Identify the preparation type.
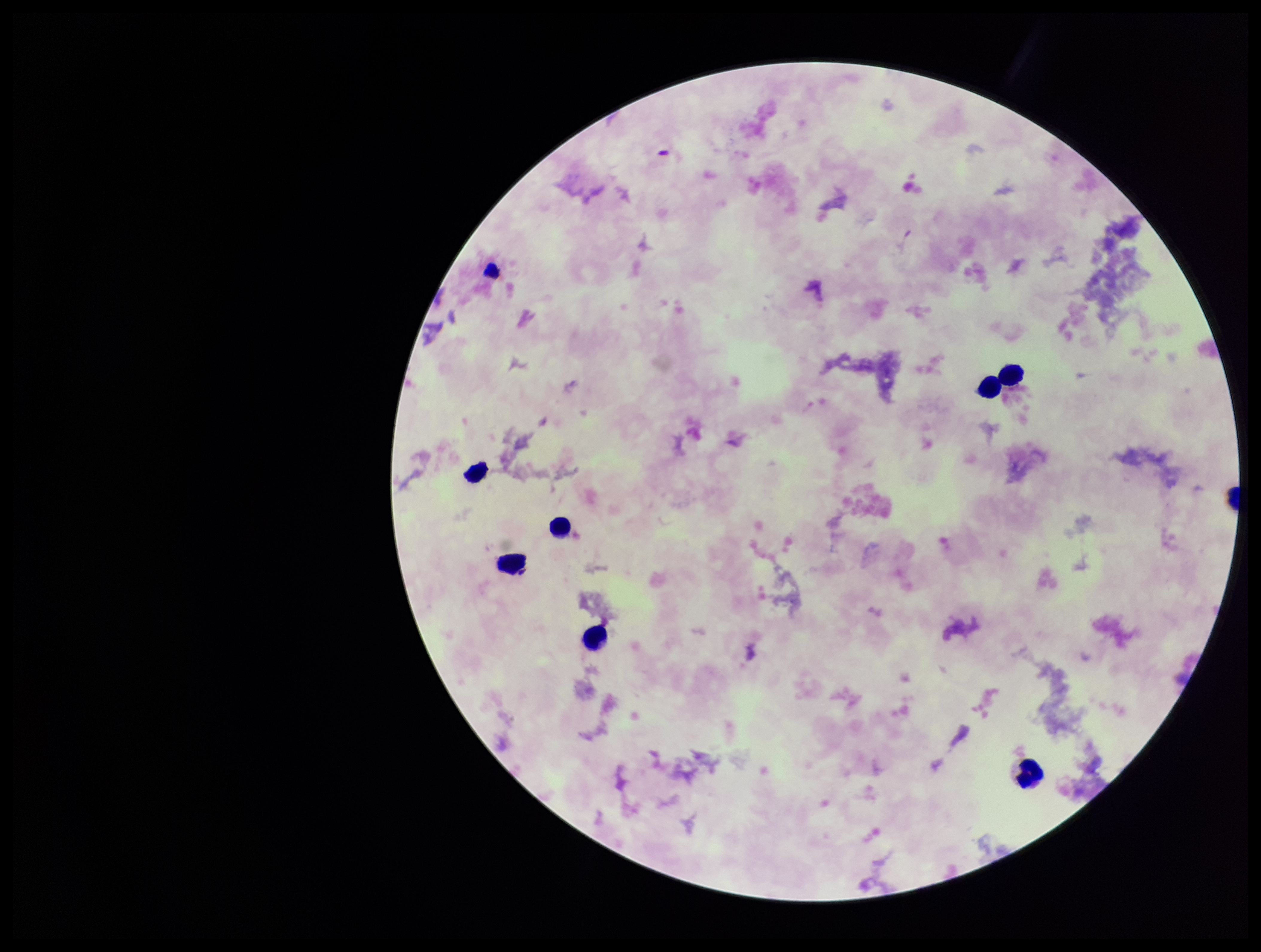
A thick smear.

{
  "parasite_count": 0,
  "patient_malaria_status": "negative",
  "capture": "smartphone photograph through the microscope eyepiece",
  "image_size": "1261×952 pixels",
  "leukocyte_count": 8,
  "stain": "Giemsa",
  "field_of_view": "single",
  "plasmodium_parasites": "none identified"
}